Give the position of every Plasmodium parasite.
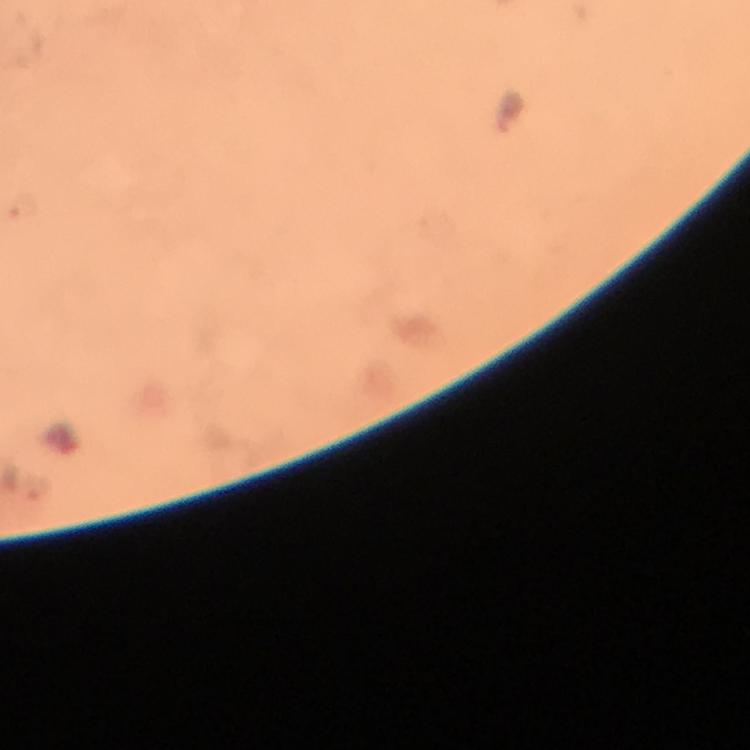
Approximate object centers, in pixels from the top-left corner.
Plasmodium parasites: (x=20, y=207).

context: from a malaria diagnostic workup
preparation: thick blood smear
magnification: 100x
stain: Giemsa
capture: smartphone mounted on the microscope
immersion_oil: applied
image_size: 750×750 pixels
cropped_from: a single field of view